Identify the parasite.
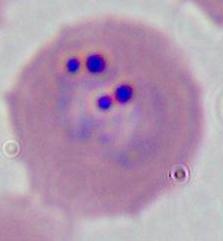

This is Plasmodium.

Summary:
  - Modality: micrograph
  - Magnification: 400x or 1000x